Report the malaria status of this cell.
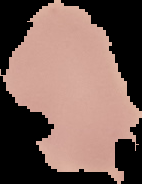
It is uninfected.

Segmented cell region on a black background. Image is 142×184 pixels. From a thin blood smear.